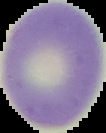

Malaria status: uninfected. From a thin blood smear. Image is 106×133 pixels. Cell region segmented out of the field of view; the surrounding area is masked to black.